Identify the blood parasite species.
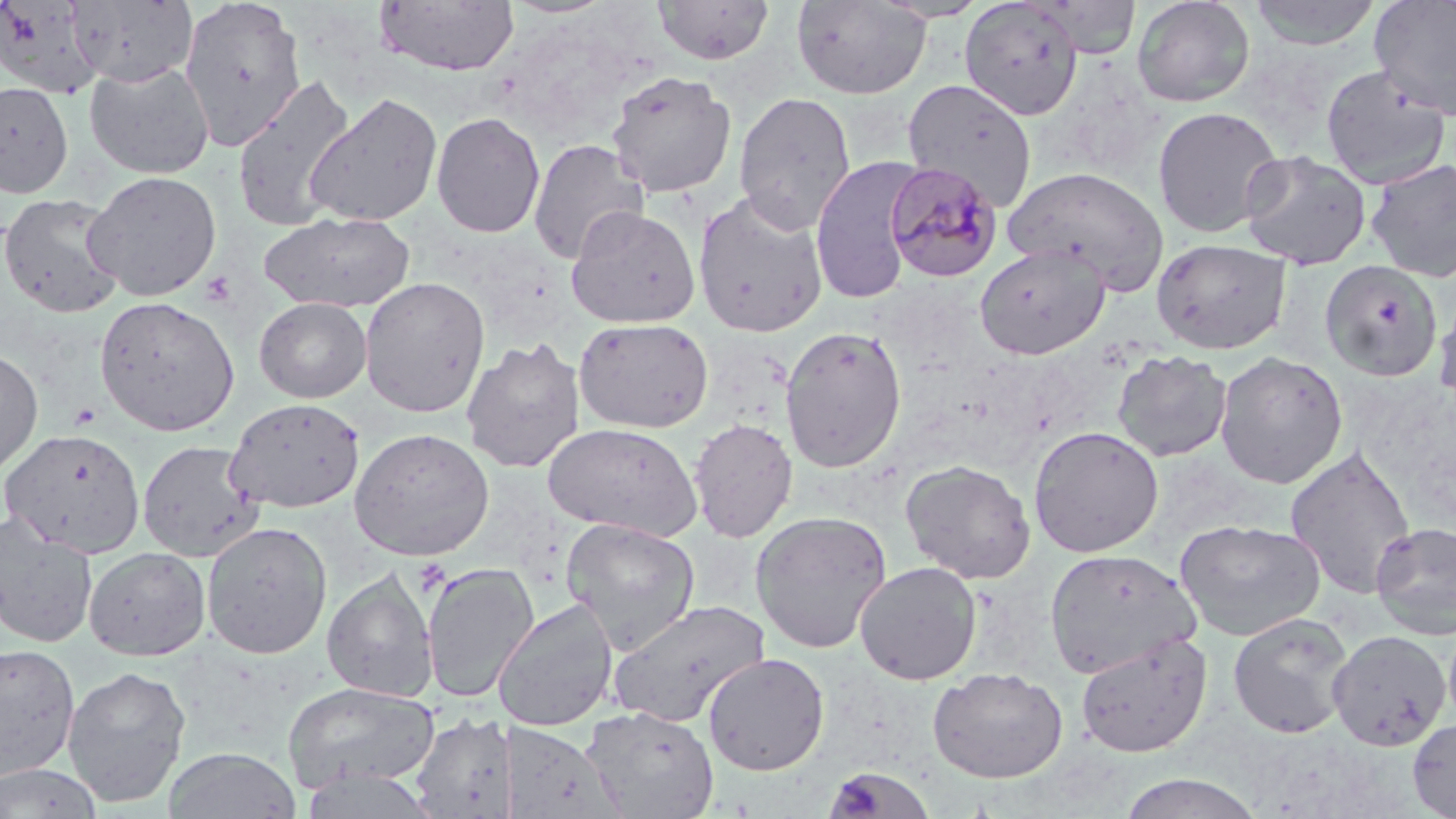
Plasmodium malariae.

Approximate bounding boxes as named x1/y1/x2/y2 corners in pixels. Platelet locations: (x1=200, y1=271, x2=237, y2=308), (x1=69, y1=401, x2=102, y2=430), (x1=828, y1=769, x2=925, y2=819). Plasmodium malariae-infected red blood cell locations: (x1=885, y1=161, x2=1004, y2=283). Uninfected red blood cell locations: (x1=66, y1=0, x2=198, y2=87), (x1=179, y1=0, x2=307, y2=150), (x1=375, y1=0, x2=520, y2=76), (x1=653, y1=0, x2=775, y2=65), (x1=791, y1=0, x2=931, y2=100), (x1=1131, y1=0, x2=1256, y2=107), (x1=1249, y1=0, x2=1382, y2=50), (x1=1369, y1=0, x2=1456, y2=120), (x1=2, y1=1, x2=106, y2=98), (x1=959, y1=1, x2=1084, y2=121), (x1=85, y1=62, x2=214, y2=179), (x1=1320, y1=66, x2=1452, y2=190), (x1=606, y1=70, x2=737, y2=199), (x1=232, y1=73, x2=356, y2=231), (x1=902, y1=78, x2=1037, y2=211), (x1=0, y1=81, x2=74, y2=199), (x1=304, y1=91, x2=443, y2=227), (x1=733, y1=91, x2=857, y2=234), (x1=1152, y1=105, x2=1283, y2=238), (x1=431, y1=111, x2=545, y2=238), (x1=527, y1=138, x2=649, y2=265), (x1=1239, y1=150, x2=1371, y2=270), (x1=809, y1=155, x2=921, y2=305), (x1=1365, y1=158, x2=1456, y2=283), (x1=1004, y1=165, x2=1169, y2=293), (x1=82, y1=170, x2=222, y2=301), (x1=0, y1=192, x2=126, y2=320), (x1=692, y1=192, x2=829, y2=339), (x1=565, y1=206, x2=700, y2=328), (x1=259, y1=210, x2=415, y2=313), (x1=1151, y1=237, x2=1292, y2=355), (x1=974, y1=243, x2=1109, y2=360), (x1=1319, y1=260, x2=1444, y2=382), (x1=358, y1=276, x2=491, y2=418), (x1=1433, y1=290, x2=1456, y2=413), (x1=94, y1=296, x2=239, y2=436), (x1=254, y1=296, x2=372, y2=403), (x1=573, y1=317, x2=714, y2=433), (x1=779, y1=325, x2=907, y2=473), (x1=461, y1=336, x2=586, y2=473), (x1=0, y1=348, x2=43, y2=477), (x1=1111, y1=349, x2=1232, y2=461), (x1=1214, y1=351, x2=1349, y2=489), (x1=224, y1=397, x2=366, y2=513), (x1=689, y1=418, x2=797, y2=542), (x1=542, y1=421, x2=702, y2=540), (x1=1028, y1=425, x2=1164, y2=557), (x1=1, y1=427, x2=147, y2=557), (x1=349, y1=427, x2=495, y2=561), (x1=137, y1=440, x2=265, y2=563), (x1=1284, y1=444, x2=1417, y2=600), (x1=900, y1=459, x2=1036, y2=584), (x1=750, y1=510, x2=892, y2=654), (x1=0, y1=512, x2=99, y2=648), (x1=560, y1=517, x2=701, y2=652), (x1=1174, y1=518, x2=1326, y2=641), (x1=201, y1=521, x2=333, y2=659), (x1=1370, y1=521, x2=1456, y2=639), (x1=83, y1=546, x2=210, y2=660), (x1=1043, y1=547, x2=1201, y2=679), (x1=854, y1=560, x2=982, y2=685), (x1=422, y1=561, x2=539, y2=703), (x1=321, y1=568, x2=439, y2=703), (x1=493, y1=598, x2=619, y2=732), (x1=607, y1=599, x2=769, y2=728), (x1=1228, y1=612, x2=1354, y2=738), (x1=1443, y1=617, x2=1456, y2=733), (x1=1327, y1=630, x2=1452, y2=750), (x1=1074, y1=632, x2=1212, y2=757), (x1=0, y1=644, x2=80, y2=780), (x1=702, y1=652, x2=830, y2=776), (x1=62, y1=664, x2=192, y2=807), (x1=927, y1=667, x2=1068, y2=783), (x1=282, y1=680, x2=441, y2=794), (x1=580, y1=705, x2=720, y2=819), (x1=409, y1=713, x2=514, y2=817), (x1=1407, y1=717, x2=1456, y2=818), (x1=505, y1=723, x2=624, y2=818), (x1=164, y1=747, x2=301, y2=819), (x1=0, y1=763, x2=103, y2=819), (x1=825, y1=765, x2=937, y2=819), (x1=1116, y1=772, x2=1267, y2=818). May-Grünwald-Giemsa-stained preparation. 1000x magnification. Image is 1456×819 pixels. Thin blood film. Optical microscopy. Single field of view.